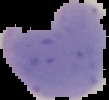

Summary:
  - Image size: 109×100 pixels
  - Preparation: thin blood smear
  - Image type: segmented cell region with the area outside set to black
  - Result: malaria parasites identified